State which parasite is depicted.
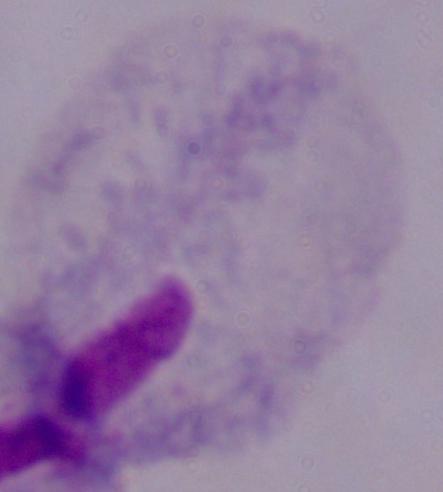

This is a trichomonad.

modality = micrograph
magnification = 1000x